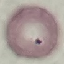
result = negative for malaria parasites
image type = cell patch, automatically extracted from a larger field of view and resized to 64 × 64 pixels
stain = Giemsa
preparation = thin blood film
capture = smartphone through the microscope eyepiece